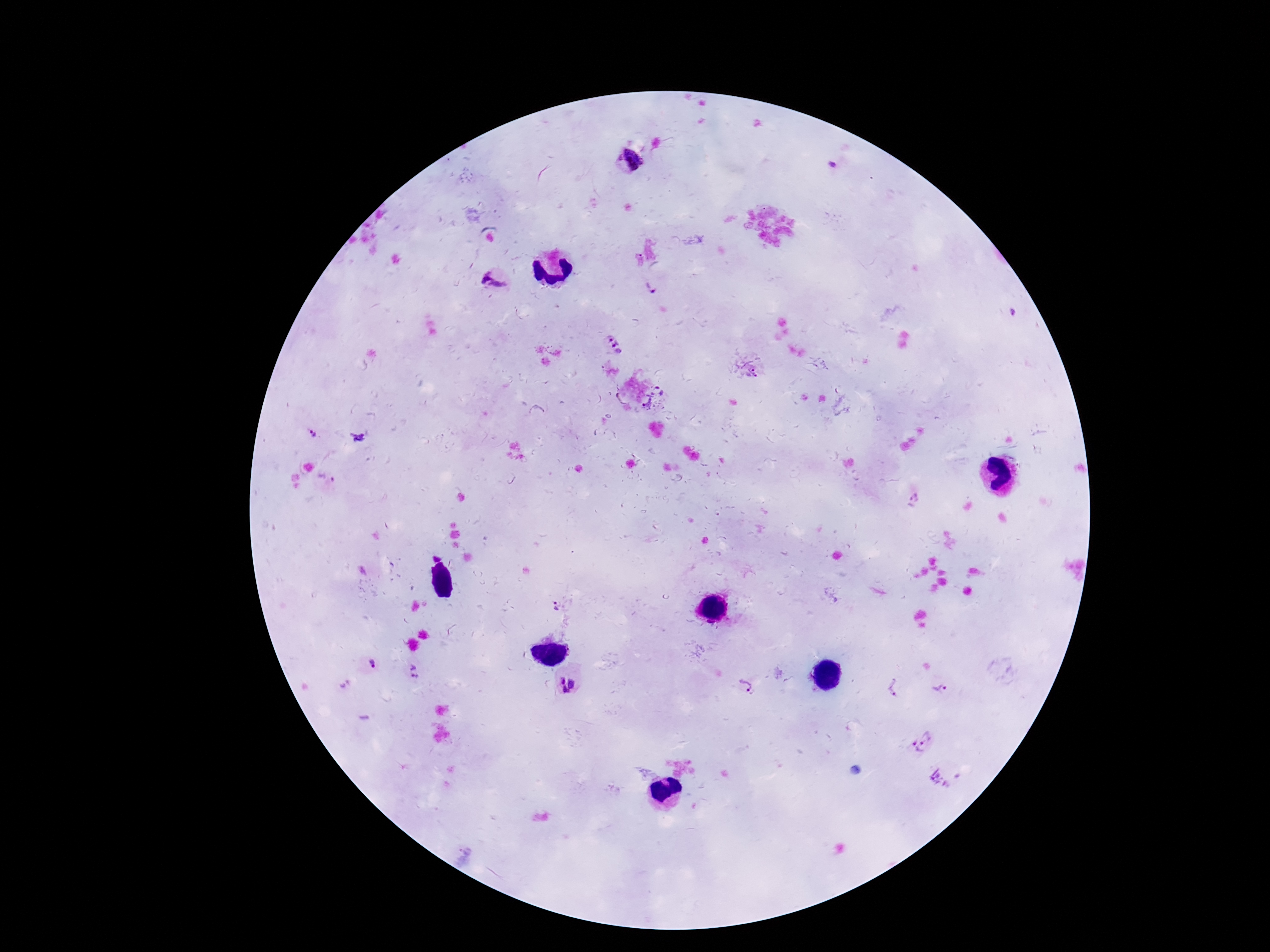
Approximate centers as (x, y) in pixels. Plasmodium parasite locations: (629, 160), (495, 278), (653, 286), (611, 344), (753, 370), (661, 404), (313, 434), (356, 438), (325, 477), (556, 607), (372, 664), (414, 673), (567, 684), (894, 687), (744, 688), (941, 689), (927, 737), (914, 751). Thick blood smear. Image is 1270×952 pixels. Photographed through the microscope eyepiece with a smartphone camera. 100x magnification. Giemsa-stained preparation. One field from this slide. Patient malaria status: infected.